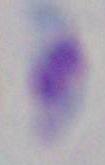
Summary:
  - Identification: Toxoplasma gondii
  - Modality: micrograph
  - Magnification: 1000x